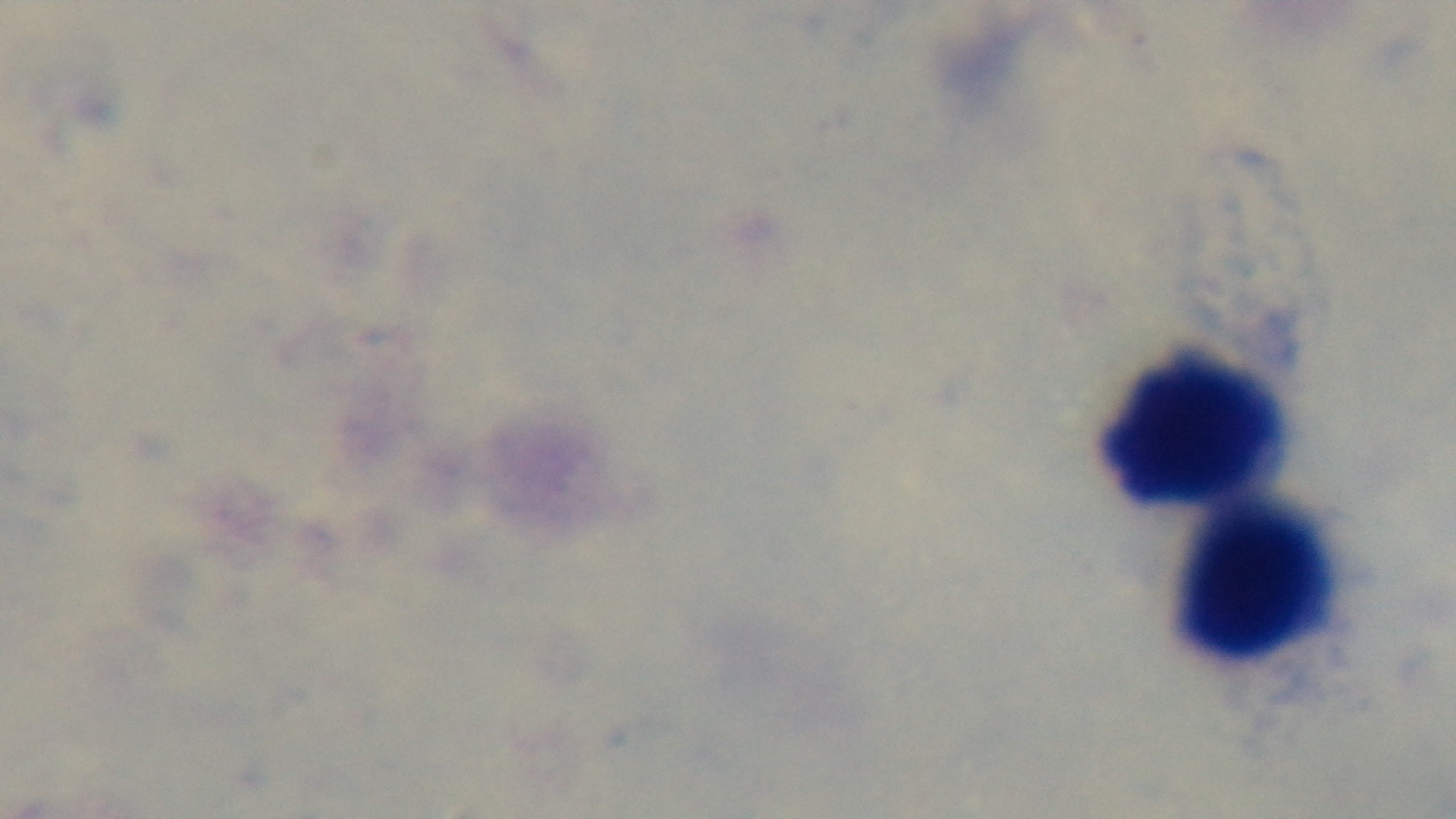

Summary:
  - Field of view: one from the slide
  - Preparation: thick
  - Capture: mounted 4K digital camera
  - Objective: 100x oil immersion
  - Stain: Giemsa
  - Malaria status: uninfected
  - Modality: light microscopy